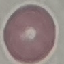

Malaria status: uninfected. Photographed with a smartphone camera at the microscope eyepiece. Thin blood smear. Giemsa-stained preparation. Cell patch, automatically extracted from a larger field of view and resized to 64 × 64 pixels.